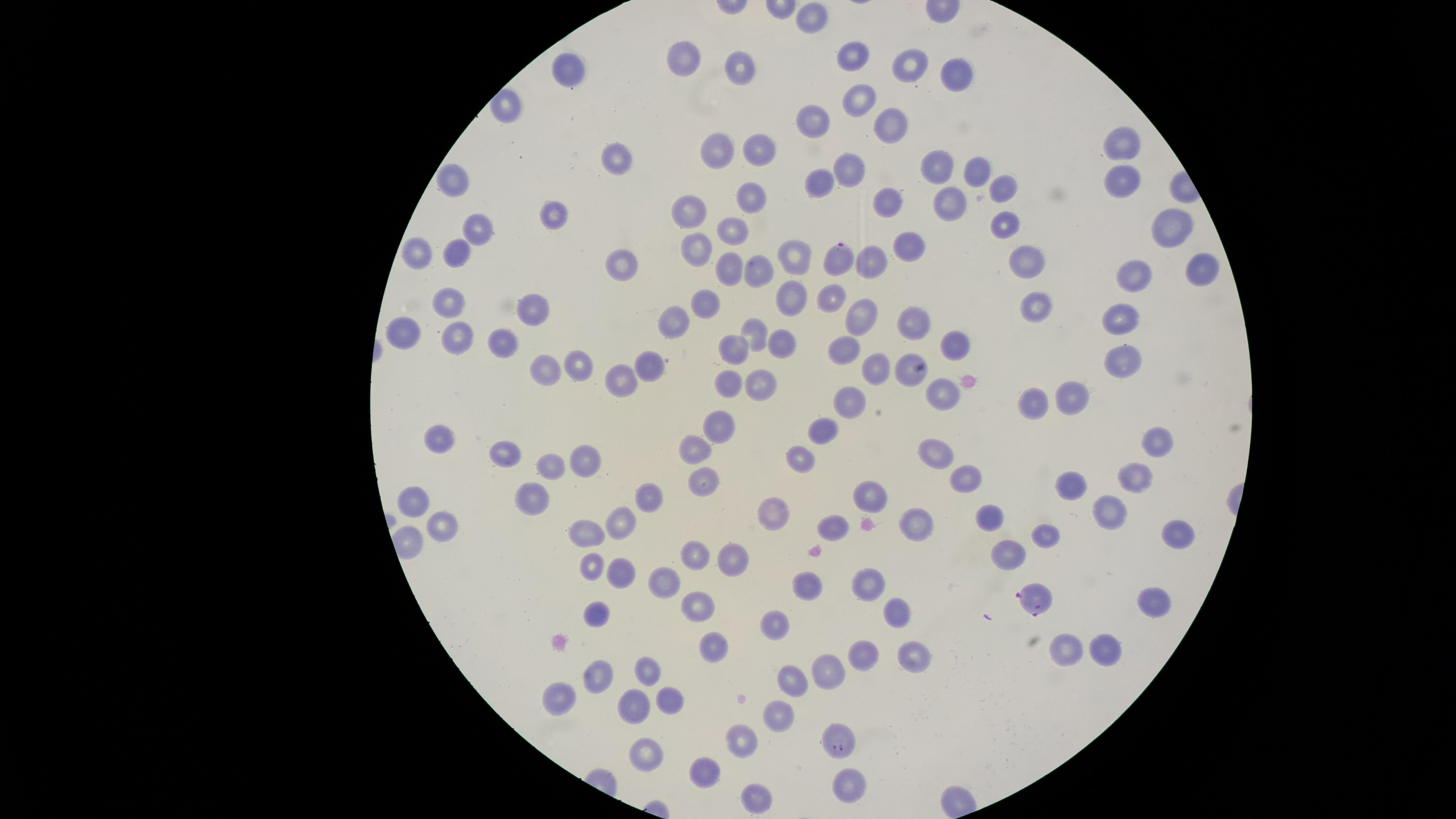
Approximate marker points as [x, y] in pixels.
Summary:
  - Parasitized red blood cells: [841, 257], [1034, 601], [841, 741]
  - Uninfected red blood cells: [817, 18], [851, 53], [686, 56], [912, 64], [745, 69], [572, 71], [957, 76], [859, 101], [815, 120], [890, 123], [1125, 140], [721, 146], [762, 152], [613, 158], [847, 166], [940, 168], [977, 169], [821, 177], [454, 178], [1120, 181], [1004, 184], [749, 197], [884, 203], [688, 207], [940, 209], [550, 210], [1009, 222], [1165, 225], [735, 227], [476, 230], [907, 245], [693, 247], [413, 251], [457, 251], [1023, 254], [794, 256], [618, 262], [873, 262], [1199, 265], [728, 268], [757, 271], [1131, 277], [830, 295], [792, 298], [451, 299], [528, 303], [1036, 307], [708, 309], [1123, 312], [675, 315], [859, 318], [912, 324], [753, 328], [409, 331], [457, 338], [502, 339], [779, 341], [955, 343], [735, 348], [844, 348], [1125, 359], [581, 365], [652, 367], [907, 368], [548, 370], [877, 370], [620, 375], [725, 380], [762, 382], [941, 394], [1066, 397], [846, 401], [1035, 401], [718, 420], [824, 430], [441, 434], [1159, 442], [694, 446], [505, 455], [935, 455], [801, 460], [583, 461], [552, 465], [1138, 474], [968, 479], [704, 480], [1073, 486], [647, 495], [528, 497], [409, 501], [872, 501], [1106, 508], [774, 514], [990, 515], [622, 521], [915, 522], [440, 525], [834, 526], [1175, 532], [585, 533], [1046, 533], [693, 553], [1007, 553], [729, 560], [586, 564], [619, 572], [665, 581], [809, 584], [872, 584], [1153, 601], [696, 608], [595, 614], [894, 614], [772, 629], [1104, 645], [711, 646], [1063, 649], [868, 654], [915, 657], [647, 669], [600, 674], [828, 674], [790, 680], [563, 694], [666, 698], [633, 707], [780, 712], [739, 740], [647, 750], [709, 770], [848, 783], [754, 798]
  - Field of view: single
  - Visible region: circular
  - Image size: 1456×819 pixels
  - Preparation: thin blood smear
  - Capture: smartphone photograph through the microscope eyepiece
  - Presence: malaria parasites identified
  - Stain: Giemsa
  - Species: Plasmodium falciparum